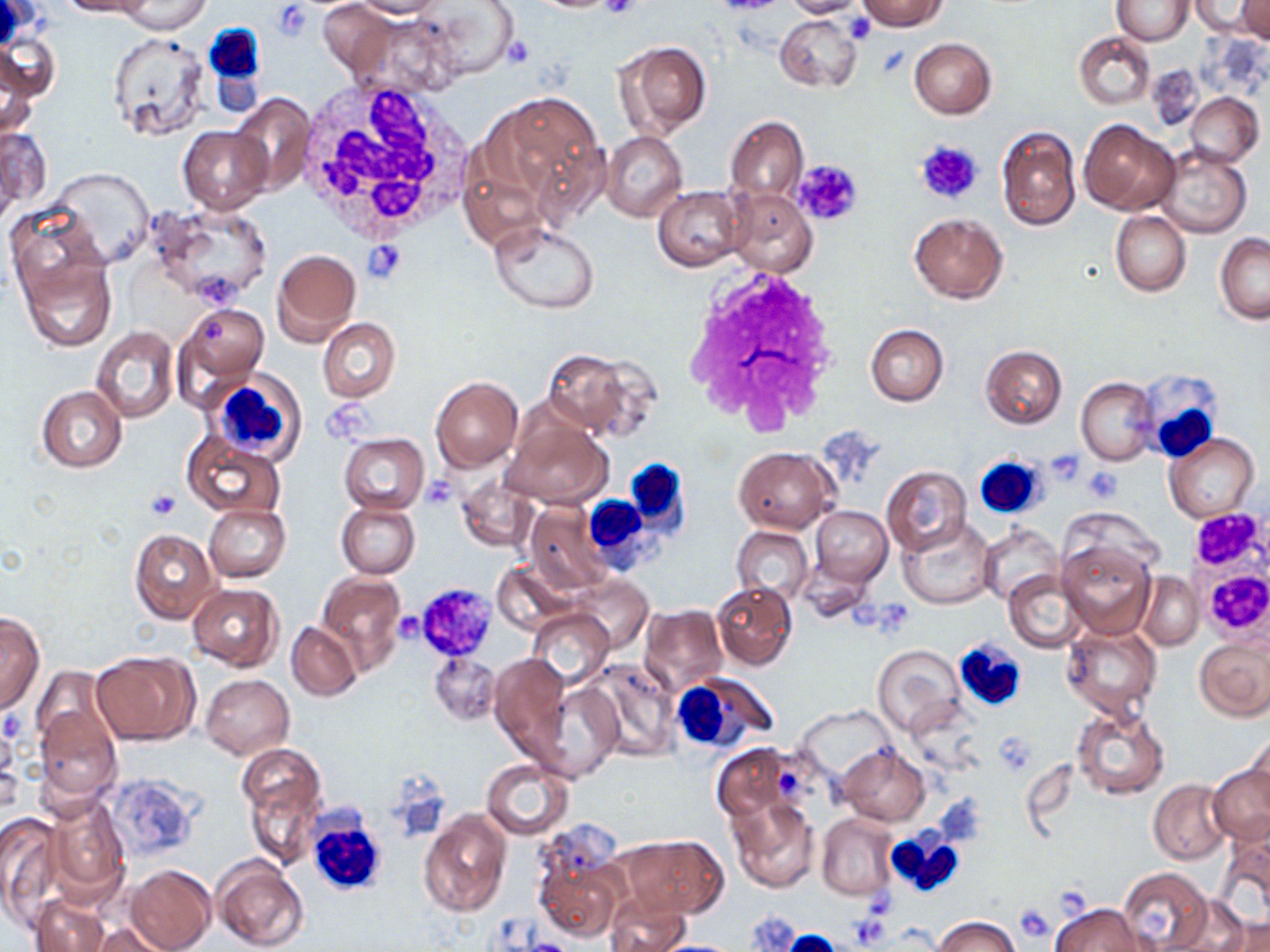
Summary:
  - Coordinate format: approximate bounding boxes as (x1, y1, x2, y2) in pixels
  - White blood cell locations: (201, 22, 266, 90), (295, 81, 472, 236), (681, 267, 843, 430), (203, 368, 307, 463), (1139, 373, 1227, 463), (974, 454, 1050, 520), (630, 458, 694, 541), (590, 491, 669, 575), (953, 637, 1027, 712), (669, 671, 777, 756), (310, 803, 387, 898), (886, 829, 966, 899)
  - Platelet locations: (600, 0, 643, 21), (273, 3, 312, 40), (846, 13, 876, 44), (504, 35, 537, 67), (915, 139, 983, 206), (794, 157, 865, 228), (362, 239, 408, 282), (1046, 449, 1088, 486), (1083, 467, 1121, 504), (419, 476, 459, 510), (148, 488, 179, 520), (415, 582, 498, 660), (392, 610, 425, 647), (994, 731, 1037, 776), (1015, 903, 1055, 942)
  - Uninfected red blood cell locations: (57, 0, 153, 18), (117, 0, 209, 33), (351, 0, 447, 18), (784, 0, 866, 17), (857, 0, 948, 30), (1113, 0, 1193, 45), (1235, 0, 1270, 44), (0, 1, 49, 49), (415, 1, 520, 79), (1188, 1, 1263, 38), (319, 2, 395, 77), (353, 12, 463, 99), (774, 15, 862, 92), (107, 30, 209, 141), (1074, 32, 1156, 111), (0, 35, 58, 102), (910, 37, 995, 118), (612, 40, 711, 139), (2, 62, 40, 140), (485, 89, 607, 213), (1184, 92, 1264, 165), (231, 94, 315, 191), (726, 116, 808, 202), (1079, 119, 1180, 215), (0, 124, 51, 217), (179, 126, 272, 214), (996, 126, 1080, 232), (602, 131, 687, 222), (1157, 146, 1252, 237), (49, 168, 154, 266), (654, 185, 747, 272), (727, 189, 818, 277), (147, 203, 273, 309), (8, 206, 108, 310), (1111, 210, 1190, 297), (910, 213, 1007, 303), (490, 221, 600, 313), (1215, 233, 1269, 324), (272, 249, 361, 347), (18, 253, 117, 351), (173, 303, 269, 401), (318, 317, 401, 401), (865, 323, 949, 406), (91, 327, 180, 423), (980, 345, 1067, 428), (542, 346, 655, 440), (431, 376, 523, 472), (1076, 376, 1157, 466), (37, 385, 126, 472), (504, 415, 613, 508), (182, 433, 284, 519), (339, 433, 429, 515), (1166, 433, 1258, 524), (734, 447, 834, 533), (881, 465, 971, 557), (455, 475, 538, 552), (336, 501, 420, 579), (524, 501, 613, 593), (204, 503, 291, 582), (810, 505, 893, 587), (898, 520, 994, 609), (979, 523, 1063, 605), (732, 526, 813, 603), (129, 528, 221, 623), (1057, 539, 1156, 639), (491, 562, 577, 635), (317, 570, 407, 671), (1004, 570, 1089, 653), (1135, 572, 1205, 650), (569, 576, 652, 654), (711, 582, 796, 669), (187, 583, 282, 671), (639, 605, 727, 695), (527, 607, 612, 687), (0, 610, 45, 716), (286, 622, 362, 701), (1061, 624, 1162, 724), (1195, 636, 1270, 722), (872, 644, 963, 736), (91, 651, 199, 745), (430, 652, 501, 724), (490, 653, 573, 758), (584, 657, 680, 761), (31, 666, 114, 759), (201, 674, 294, 758), (538, 681, 624, 782), (907, 699, 986, 774), (35, 704, 122, 808), (1070, 705, 1170, 800), (796, 706, 895, 783), (0, 719, 23, 813), (1246, 733, 1270, 816), (711, 743, 797, 820), (238, 745, 326, 868), (838, 745, 930, 826), (480, 759, 574, 839), (1207, 763, 1269, 846), (379, 770, 452, 842), (1149, 778, 1232, 865), (43, 791, 131, 904), (726, 794, 820, 894), (419, 811, 511, 916), (816, 812, 898, 900), (0, 813, 65, 931), (1217, 826, 1270, 928), (622, 834, 728, 919), (535, 856, 623, 943), (212, 858, 310, 952), (125, 864, 217, 952), (1118, 866, 1213, 951), (32, 892, 110, 952), (606, 894, 691, 952), (1051, 902, 1145, 951), (744, 911, 803, 951), (933, 915, 1023, 952), (1216, 915, 1270, 952), (91, 920, 174, 951)
  - Slide-level diagnosis: no evidence of blood parasites
  - Stain: May-Grünwald-Giemsa
  - Modality: optical microscopy
  - Image size: 1270×952 pixels
  - Magnification: 1000x
  - Field of view: single
  - Preparation: thin blood smear